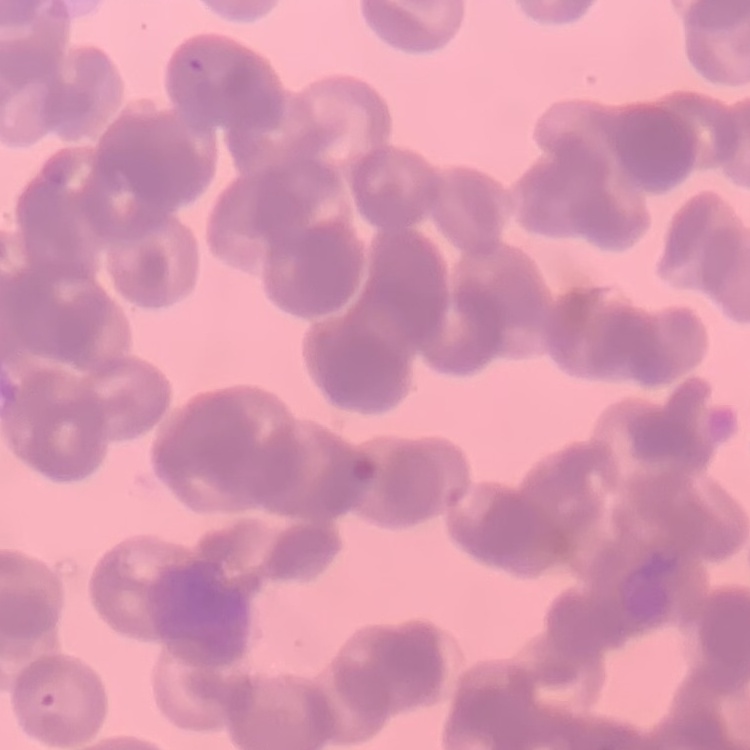
{
  "erythrocyte_morphology": "rouleaux formation",
  "stain": "Field's or Giemsa",
  "image_type": "square crop of a larger photomicrograph",
  "preparation": "thin blood film"
}